Name the cell type shown.
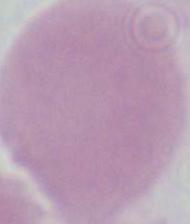

This is an erythrocyte.

modality: photomicrograph
magnification: 1000x